Outline each uninfected red blood cell.
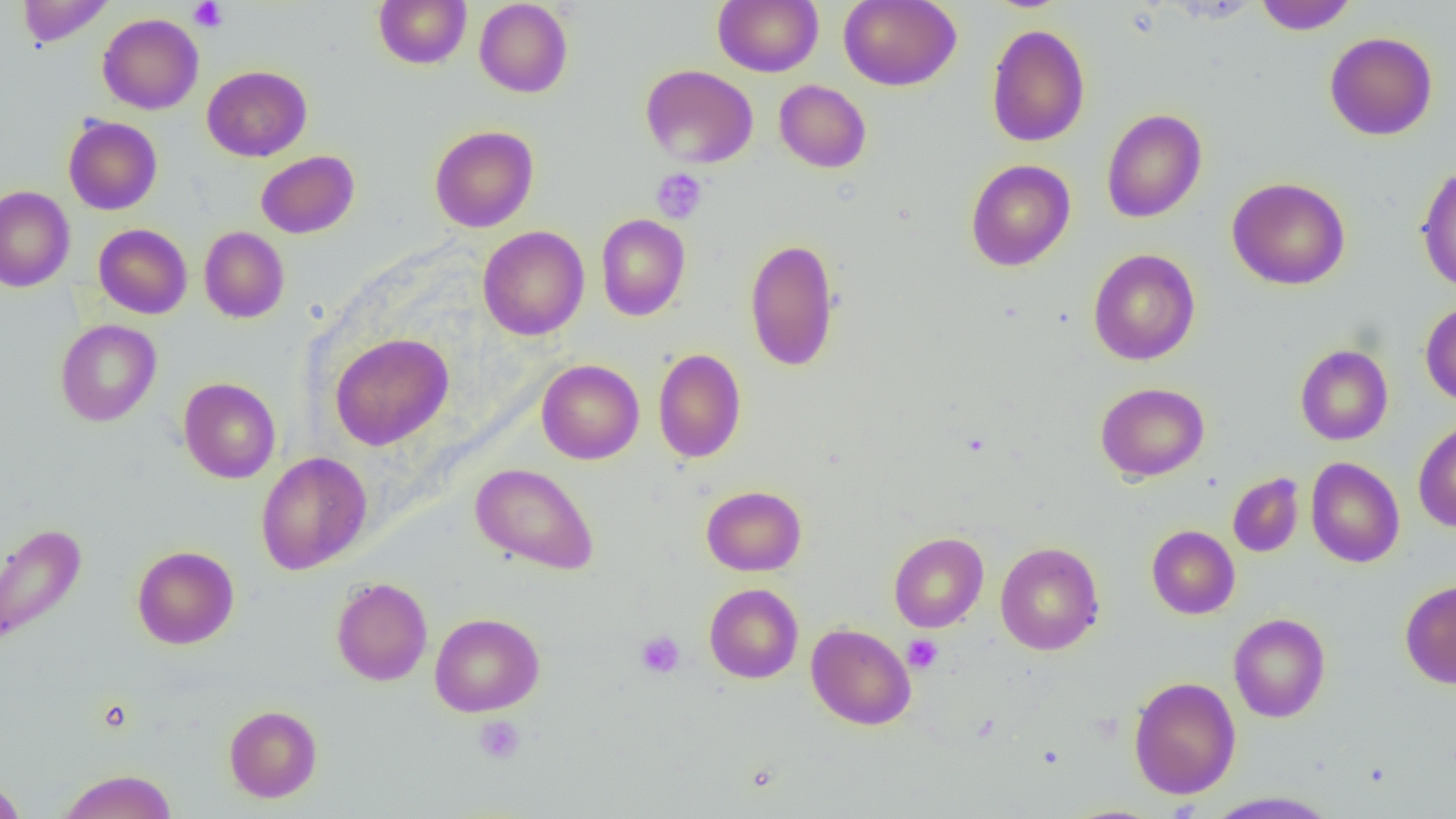

Approximate bounding boxes as named x1/y1/x2/y2 corners in pixels.
Uninfected red blood cells: (x1=17, y1=0, x2=115, y2=47), (x1=374, y1=0, x2=471, y2=69), (x1=474, y1=0, x2=573, y2=98), (x1=713, y1=0, x2=823, y2=76), (x1=839, y1=0, x2=961, y2=90), (x1=1254, y1=0, x2=1357, y2=34), (x1=97, y1=13, x2=203, y2=114), (x1=986, y1=23, x2=1090, y2=147), (x1=1324, y1=32, x2=1437, y2=140), (x1=641, y1=64, x2=758, y2=168), (x1=202, y1=65, x2=312, y2=161), (x1=774, y1=79, x2=871, y2=173), (x1=1101, y1=108, x2=1207, y2=223), (x1=63, y1=116, x2=162, y2=215), (x1=429, y1=125, x2=539, y2=232), (x1=256, y1=151, x2=359, y2=238), (x1=965, y1=159, x2=1076, y2=271), (x1=1416, y1=164, x2=1456, y2=293), (x1=1227, y1=177, x2=1350, y2=290), (x1=0, y1=186, x2=75, y2=292), (x1=596, y1=213, x2=690, y2=320), (x1=94, y1=223, x2=192, y2=319), (x1=478, y1=226, x2=589, y2=340), (x1=199, y1=227, x2=289, y2=323), (x1=744, y1=238, x2=840, y2=371), (x1=1088, y1=248, x2=1200, y2=365), (x1=1420, y1=301, x2=1456, y2=407), (x1=55, y1=319, x2=161, y2=426), (x1=330, y1=333, x2=453, y2=450), (x1=1295, y1=344, x2=1393, y2=445), (x1=653, y1=348, x2=746, y2=463), (x1=537, y1=359, x2=644, y2=464), (x1=178, y1=377, x2=281, y2=483), (x1=1095, y1=382, x2=1210, y2=482), (x1=1413, y1=419, x2=1456, y2=532), (x1=256, y1=451, x2=371, y2=575), (x1=1306, y1=457, x2=1404, y2=568), (x1=471, y1=463, x2=599, y2=574), (x1=1227, y1=472, x2=1304, y2=557), (x1=701, y1=485, x2=806, y2=575), (x1=0, y1=522, x2=87, y2=647), (x1=1147, y1=525, x2=1240, y2=619), (x1=889, y1=532, x2=989, y2=632), (x1=995, y1=541, x2=1104, y2=655), (x1=132, y1=545, x2=239, y2=649), (x1=331, y1=577, x2=433, y2=685), (x1=1400, y1=580, x2=1456, y2=689), (x1=704, y1=583, x2=803, y2=683), (x1=429, y1=612, x2=544, y2=717), (x1=1228, y1=613, x2=1330, y2=722), (x1=806, y1=624, x2=916, y2=730), (x1=1128, y1=676, x2=1241, y2=799), (x1=224, y1=705, x2=322, y2=803), (x1=57, y1=769, x2=177, y2=819), (x1=0, y1=777, x2=27, y2=818), (x1=1203, y1=791, x2=1341, y2=818).

slide_level_diagnosis: no evidence of blood parasites
magnification: 1000x
modality: light microscopy
preparation: thin blood smear
platelet_locations: 'approximate bounding boxes as named x1/y1/x2/y2 corners in pixels: (x1=188, y1=0, x2=227, y2=32), (x1=652, y1=168, x2=707, y2=223), (x1=636, y1=631, x2=684, y2=679), (x1=902, y1=633, x2=943, y2=673), (x1=474, y1=715, x2=526, y2=764)'
field_of_view: single
image_size: 1456×819 pixels